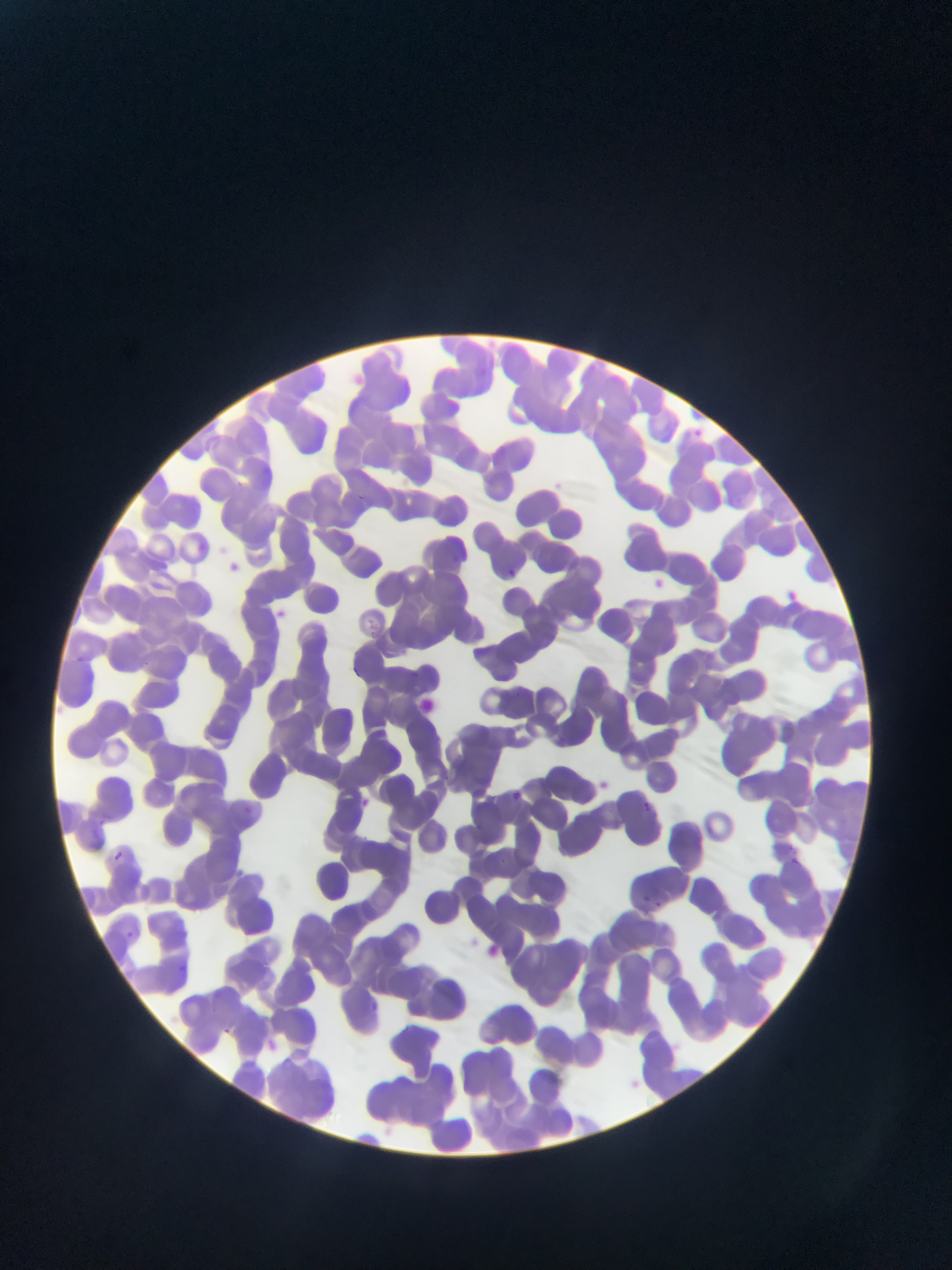 Approximate bounding boxes as (left, top, right, bottom) in pixels. Plasmodium parasite locations: (226, 555, 243, 574), (505, 567, 531, 591), (648, 574, 663, 598), (508, 789, 525, 806), (643, 800, 652, 810), (246, 802, 259, 814), (99, 811, 112, 831), (789, 853, 800, 866), (637, 893, 656, 908), (126, 930, 134, 938) | approximate (x, y) pixel centers of objects too small to bound: (117, 856). Thin blood smear. Image is 952×1270 pixels. Sample from Ghana. Mobile-phone photograph taken through the microscope. One field of view.